Give the extent of all Plasmodium vivax-infected red blood cells.
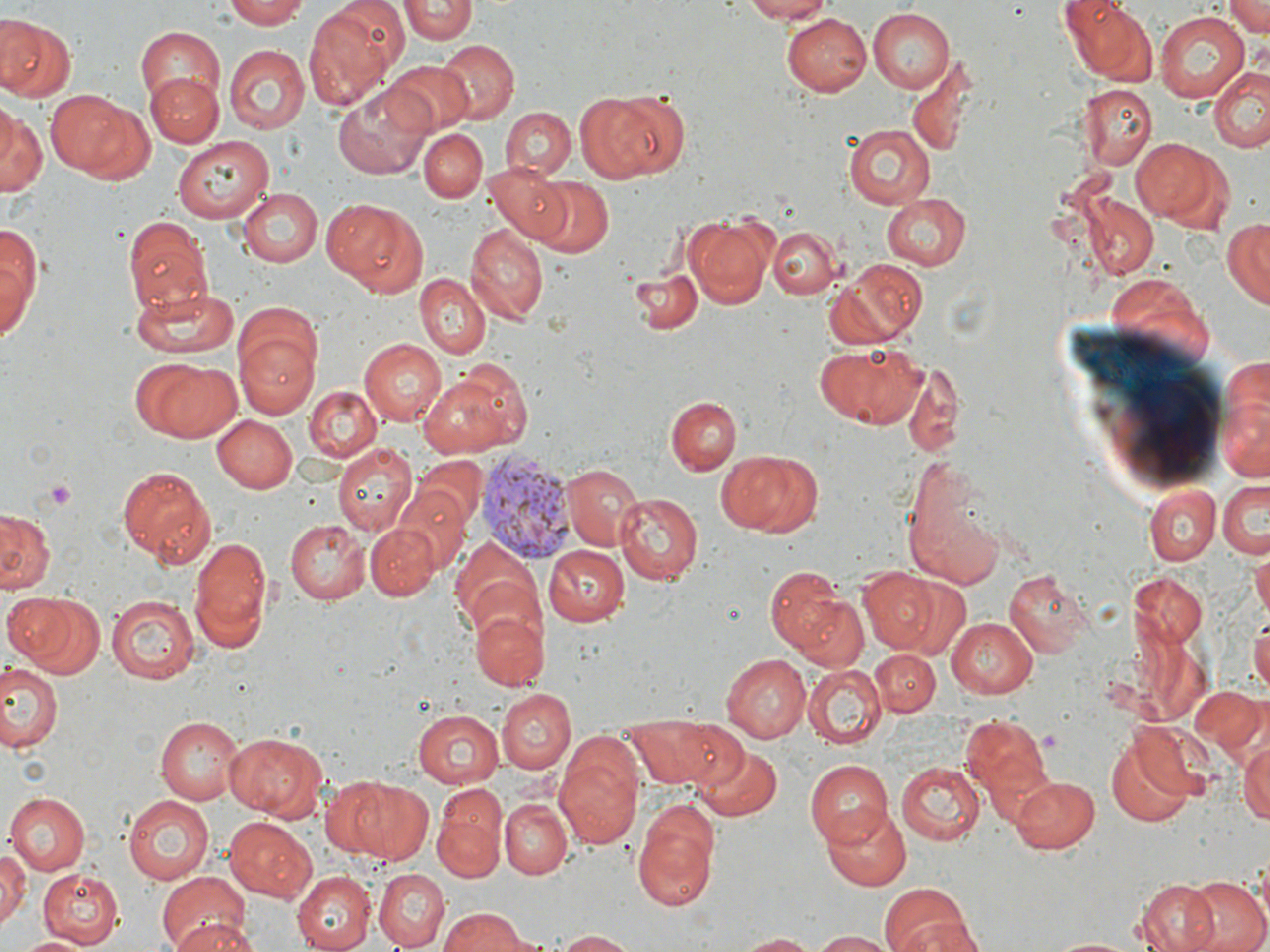
Approximate bounding boxes as (x1,y1)-(x2,y2) corner pairs in pixels.
Plasmodium vivax-infected red blood cells: (477,450)-(576,564).

slide-level diagnosis = Plasmodium vivax
field of view = single
image size = 1270×952 pixels
stain = May-Grünwald-Giemsa
modality = light microscopy
uninfected red blood cell locations = approximate bounding boxes as (x1,y1)-(x2,y2) corner pairs in pixels: (222,0)-(312,28), (737,0)-(839,23), (1225,0)-(1269,38), (1067,1)-(1156,86), (401,2)-(477,44), (302,3)-(404,113), (867,8)-(955,93), (1153,11)-(1252,104), (784,12)-(874,96), (0,18)-(75,102), (135,26)-(226,115), (438,40)-(518,122), (225,45)-(307,133), (906,53)-(981,160), (387,60)-(476,132), (1209,64)-(1269,151), (146,73)-(222,146), (858,78)-(968,187), (334,81)-(434,177), (1077,85)-(1157,169), (574,86)-(679,182), (50,89)-(145,180), (0,104)-(43,203), (502,108)-(574,181), (841,123)-(933,210), (419,129)-(487,202), (171,135)-(272,224), (1132,137)-(1224,226), (484,162)-(574,248), (533,177)-(613,256), (237,188)-(322,267), (880,193)-(971,270), (1078,195)-(1159,281), (321,199)-(426,295), (122,214)-(215,313), (685,214)-(773,307), (1223,216)-(1269,309), (466,222)-(547,325), (0,223)-(40,335), (768,225)-(839,300), (826,258)-(926,349), (629,264)-(704,334), (414,273)-(489,358), (129,287)-(239,359), (235,333)-(320,421), (359,338)-(445,425), (814,340)-(926,428), (133,358)-(244,444), (902,364)-(966,458), (421,374)-(518,455), (303,385)-(382,463), (1217,390)-(1269,488), (666,395)-(740,475), (213,413)-(299,493), (331,442)-(416,536), (713,450)-(818,535), (414,455)-(488,533), (559,464)-(640,553), (117,466)-(217,566), (902,475)-(1004,586), (1219,478)-(1269,558), (1144,483)-(1220,564), (393,485)-(473,574), (613,491)-(701,583), (0,510)-(53,595), (285,520)-(370,605), (366,523)-(440,601), (187,531)-(273,652), (544,544)-(628,626), (453,545)-(545,641), (1253,549)-(1270,619), (765,562)-(860,664), (855,565)-(941,654), (1002,567)-(1093,658), (1130,570)-(1207,649), (887,574)-(969,657), (4,592)-(103,676), (105,594)-(199,684), (470,604)-(548,689), (1250,611)-(1270,698), (946,616)-(1038,696), (870,648)-(938,718), (723,653)-(810,740), (0,663)-(61,753), (803,663)-(887,749), (1190,686)-(1266,757), (496,688)-(576,773), (414,708)-(509,789), (959,711)-(1053,813), (623,714)-(730,788), (155,717)-(244,804), (1237,730)-(1270,829), (227,733)-(327,819), (1104,736)-(1199,828), (693,745)-(782,820), (553,749)-(644,849), (804,760)-(893,848), (897,760)-(984,846), (1009,775)-(1099,853), (329,778)-(435,864), (8,791)-(91,874), (123,794)-(214,882), (433,795)-(506,882), (501,799)-(570,878), (820,803)-(911,890), (633,807)-(720,912), (224,817)-(317,902), (0,848)-(28,928), (39,870)-(125,947), (294,870)-(376,952), (373,870)-(449,948), (156,872)-(252,952), (1176,875)-(1270,952), (1133,879)-(1220,952), (879,884)-(973,952), (438,909)-(532,952), (168,915)-(260,952), (551,930)-(643,951), (808,931)-(896,951), (733,932)-(820,951), (17,935)-(92,952), (1044,935)-(1143,951)
magnification = 1000x
preparation = thin blood smear
platelet locations = approximate bounding boxes as (x1,y1)-(x2,y2) corner pairs in pixels: (39,479)-(78,511)